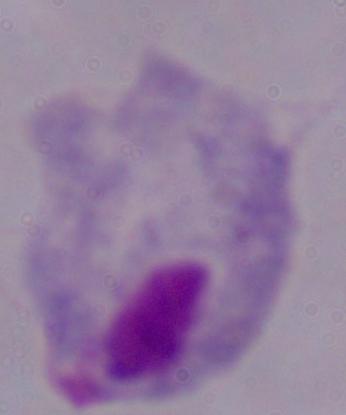

A trichomonad is seen. 1000x magnification. Photomicrograph.